Identify the blood parasite species.
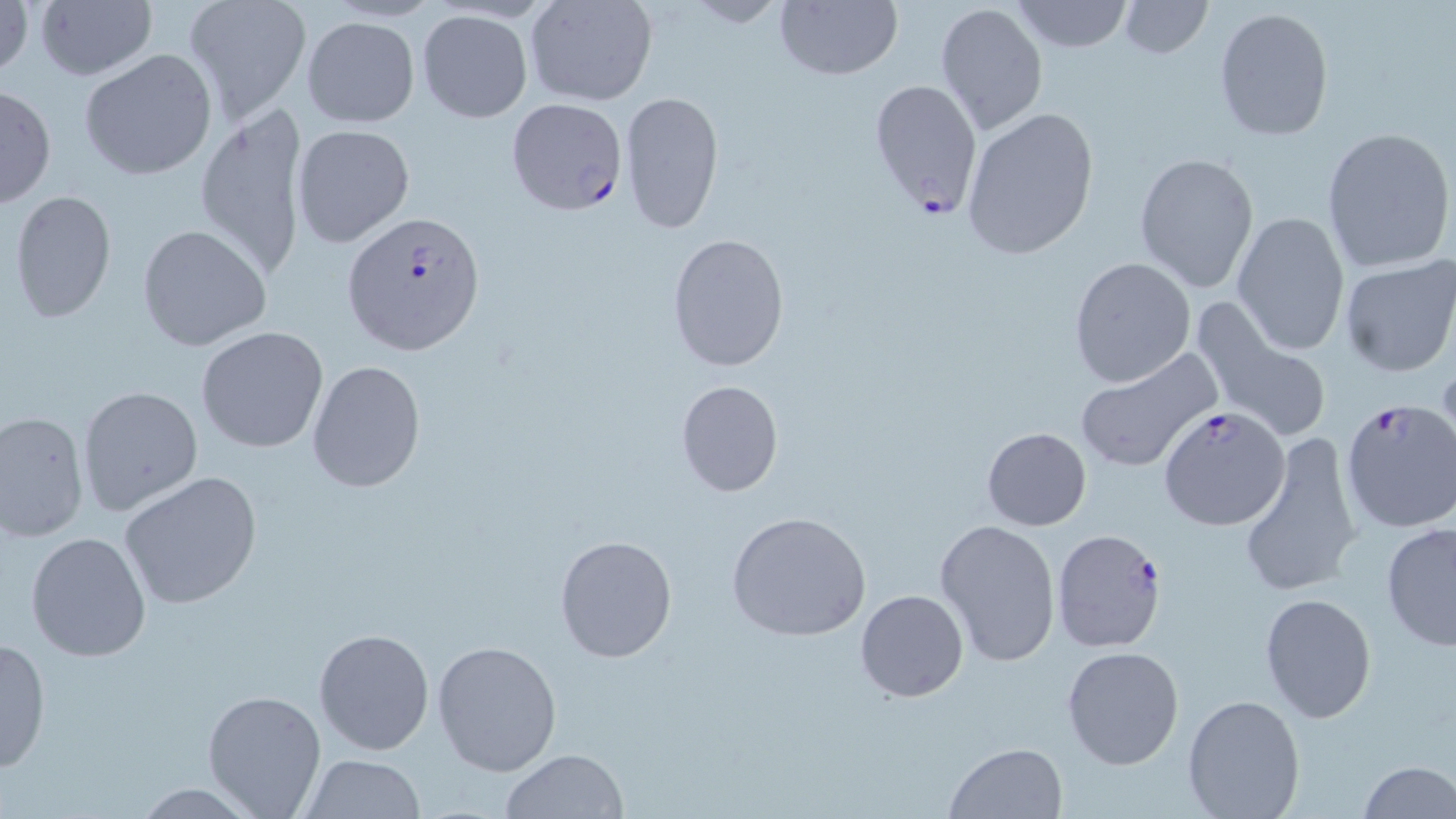
Plasmodium falciparum.

Approximate bounding boxes as (x1, y1, x2, y2) in pixels. Plasmodium falciparum-infected red blood cell locations: (869, 79, 985, 220), (506, 98, 627, 216), (341, 210, 486, 358), (1342, 396, 1456, 533), (1158, 409, 1298, 537), (1052, 528, 1171, 651). Uninfected red blood cell locations: (1, 0, 33, 85), (181, 0, 311, 123), (682, 0, 784, 29), (775, 0, 902, 80), (1010, 0, 1135, 53), (526, 1, 658, 106), (935, 1, 1048, 135), (1117, 1, 1211, 59), (34, 2, 157, 82), (1213, 6, 1334, 143), (416, 9, 533, 123), (300, 15, 419, 128), (78, 47, 218, 182), (0, 82, 56, 210), (620, 90, 725, 233), (195, 103, 311, 277), (960, 104, 1100, 261), (292, 124, 417, 250), (1321, 125, 1455, 273), (1133, 152, 1260, 294), (8, 188, 119, 324), (1231, 211, 1350, 356), (137, 224, 272, 353), (667, 234, 790, 370), (1338, 255, 1456, 378), (1068, 256, 1197, 389), (1190, 297, 1333, 445), (195, 327, 329, 453), (1074, 347, 1223, 475), (306, 359, 427, 494), (676, 380, 784, 499), (77, 386, 204, 519), (0, 409, 90, 544), (981, 427, 1092, 531), (1237, 430, 1362, 600), (117, 471, 264, 611), (724, 511, 872, 642), (934, 518, 1061, 667), (1380, 522, 1456, 651), (24, 530, 154, 663), (553, 533, 678, 664), (855, 588, 969, 703), (1260, 593, 1376, 722), (313, 627, 435, 755), (1, 637, 52, 775), (431, 638, 563, 775), (1062, 645, 1184, 770), (201, 689, 327, 816), (1182, 693, 1305, 819), (945, 741, 1068, 818), (500, 749, 628, 819), (297, 754, 427, 818), (1357, 760, 1456, 819). Single field of view. Light microscopy. Captured at 1000x magnification. Image is 1456×819 pixels. May-Grünwald-Giemsa-stained preparation. Thin blood smear.